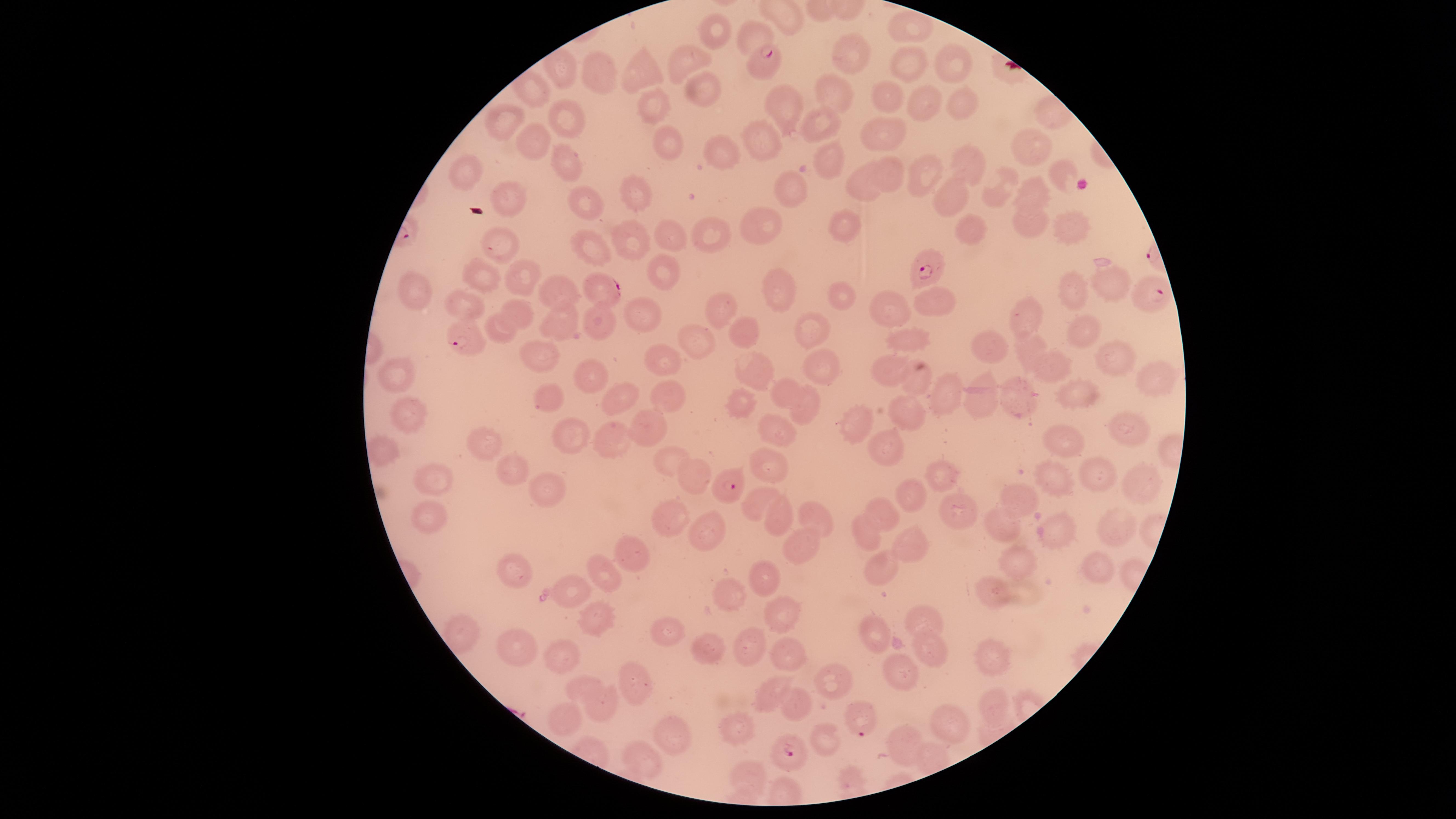
Approximate marker points, in pixels from the top-left corner. Uninfected RBCs: (x=907, y=25), (x=720, y=31), (x=752, y=38), (x=853, y=54), (x=690, y=63), (x=911, y=63), (x=954, y=63), (x=642, y=74), (x=601, y=79), (x=708, y=91), (x=840, y=93), (x=882, y=100), (x=962, y=100), (x=654, y=103), (x=788, y=103), (x=927, y=105), (x=567, y=118), (x=510, y=124), (x=826, y=128), (x=885, y=131), (x=669, y=141), (x=765, y=142), (x=540, y=149), (x=1034, y=149), (x=563, y=156), (x=723, y=158), (x=834, y=162), (x=970, y=163), (x=461, y=171), (x=1059, y=172), (x=929, y=173), (x=893, y=174), (x=862, y=186), (x=1001, y=190), (x=798, y=191), (x=1037, y=192), (x=638, y=197), (x=513, y=198), (x=585, y=199), (x=955, y=199), (x=757, y=222), (x=1075, y=226), (x=846, y=227), (x=1031, y=227), (x=971, y=231), (x=712, y=232), (x=635, y=235), (x=500, y=240), (x=674, y=240), (x=587, y=250), (x=665, y=265), (x=490, y=284), (x=523, y=284), (x=1114, y=285), (x=783, y=291), (x=424, y=295), (x=1074, y=295), (x=562, y=296), (x=843, y=299), (x=943, y=304), (x=471, y=307), (x=889, y=307), (x=716, y=309), (x=519, y=310), (x=1031, y=315), (x=643, y=320), (x=601, y=323), (x=812, y=327), (x=562, y=328), (x=510, y=330), (x=1082, y=333), (x=912, y=334), (x=745, y=335), (x=699, y=340), (x=998, y=347), (x=1031, y=353), (x=1112, y=355), (x=665, y=362), (x=546, y=363), (x=1060, y=367), (x=753, y=369), (x=890, y=369), (x=820, y=371), (x=599, y=374), (x=1156, y=374), (x=398, y=379), (x=920, y=382), (x=787, y=391), (x=549, y=393), (x=949, y=394), (x=668, y=395), (x=1019, y=395), (x=1082, y=396), (x=618, y=398), (x=980, y=398), (x=740, y=409), (x=803, y=410), (x=409, y=417), (x=905, y=423), (x=859, y=428), (x=646, y=431), (x=778, y=431), (x=1128, y=434), (x=579, y=441), (x=612, y=443), (x=1074, y=445), (x=483, y=447), (x=883, y=456), (x=671, y=460), (x=515, y=467), (x=772, y=470), (x=1108, y=476), (x=940, y=478), (x=435, y=479), (x=695, y=480), (x=1054, y=483), (x=1136, y=483), (x=546, y=494), (x=1026, y=500), (x=906, y=502), (x=757, y=503), (x=957, y=507), (x=816, y=516), (x=882, y=516), (x=779, y=518), (x=429, y=520), (x=670, y=524), (x=1005, y=526), (x=1118, y=528), (x=1066, y=530), (x=702, y=535), (x=869, y=536), (x=797, y=546), (x=907, y=546), (x=637, y=553), (x=1015, y=564), (x=1093, y=564), (x=883, y=569), (x=523, y=572), (x=603, y=572), (x=771, y=577), (x=992, y=587), (x=574, y=592), (x=729, y=593), (x=596, y=617), (x=783, y=618), (x=923, y=619), (x=879, y=635), (x=667, y=636), (x=750, y=642), (x=705, y=646), (x=513, y=647), (x=928, y=651), (x=565, y=653), (x=995, y=653), (x=787, y=658), (x=904, y=674), (x=834, y=679), (x=634, y=687), (x=584, y=688), (x=775, y=690), (x=796, y=703), (x=992, y=703), (x=604, y=713), (x=573, y=720), (x=951, y=725), (x=674, y=731), (x=737, y=733), (x=825, y=743), (x=910, y=746), (x=642, y=761), (x=749, y=775). Parasitized RBCs: (x=766, y=62), (x=929, y=266), (x=599, y=291), (x=1151, y=297), (x=465, y=339), (x=731, y=486), (x=857, y=717), (x=789, y=751). Image is 1456×819 pixels. Thin blood film. Giemsa-stained preparation. Species: Plasmodium falciparum. Smartphone photograph through the microscope eyepiece. The visible region is circular. One field of view of the specimen. Presence: malaria parasites detected.